Report the malaria status of this cell.
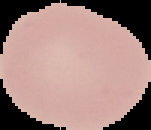

Uninfected.

Summary:
  - Preparation: thin blood smear
  - Image size: 151×130 pixels
  - Image type: segmented cell region on a black background